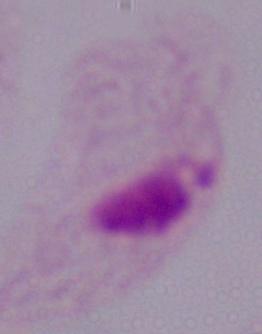 A trichomonad is shown. 1000x magnification. Micrograph.